Identify the blood parasite species.
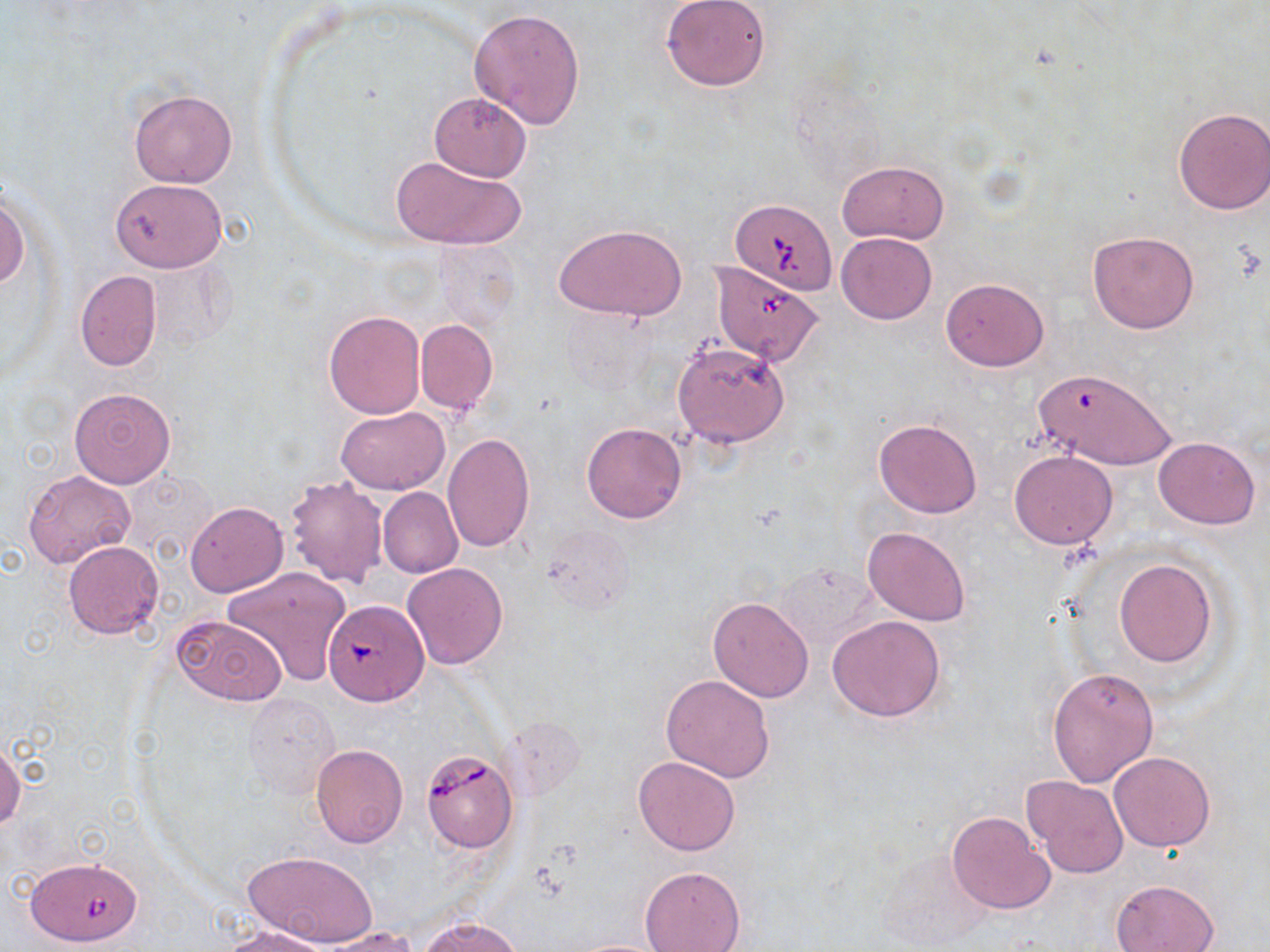
Babesia divergens.

field of view = one of a larger specimen
image size = 1270×952 pixels
Babesia divergens-infected red blood cell locations = approximate bounding boxes as (x1,y1)-(x2,y2) corner pairs in pixels: (731,199)-(836,292), (709,259)-(825,368), (323,597)-(428,705), (421,750)-(518,852), (22,861)-(149,950)
magnification = 1000x
preparation = thin blood film
stain = May-Grünwald-Giemsa
uninfected red blood cell locations = approximate bounding boxes as (x1,y1)-(x2,y2) corner pairs in pixels: (661,0)-(770,91), (469,9)-(586,131), (129,88)-(238,188), (429,92)-(532,182), (1173,107)-(1270,214), (390,154)-(526,251), (837,160)-(950,245), (111,178)-(227,272), (0,194)-(28,290), (555,223)-(687,323), (836,232)-(936,325), (1087,232)-(1200,333), (437,241)-(520,333), (75,271)-(161,371), (940,277)-(1048,371), (561,305)-(656,399), (324,310)-(426,417), (415,319)-(498,416), (673,341)-(789,448), (1031,375)-(1177,469), (69,387)-(175,488), (336,407)-(449,494), (873,419)-(983,519), (580,423)-(687,523), (441,434)-(535,553), (1154,436)-(1260,530), (1009,451)-(1118,549), (24,469)-(135,569), (283,475)-(389,589), (378,488)-(463,578), (185,501)-(288,598), (862,526)-(971,626), (63,541)-(163,639), (1115,559)-(1217,667), (402,562)-(509,669), (773,563)-(879,653), (224,566)-(352,687), (707,596)-(814,702), (172,614)-(287,706), (828,615)-(948,723), (1047,665)-(1160,787), (660,673)-(775,782), (245,691)-(341,801), (0,743)-(23,833), (310,744)-(408,849), (1108,751)-(1217,851), (633,756)-(740,855), (1022,776)-(1128,879), (947,810)-(1054,914), (242,849)-(377,949), (640,866)-(746,952), (1111,877)-(1220,952), (423,916)-(521,952), (220,924)-(334,952), (320,927)-(418,952), (565,938)-(676,951)
modality = optical microscopy